State the preparation type.
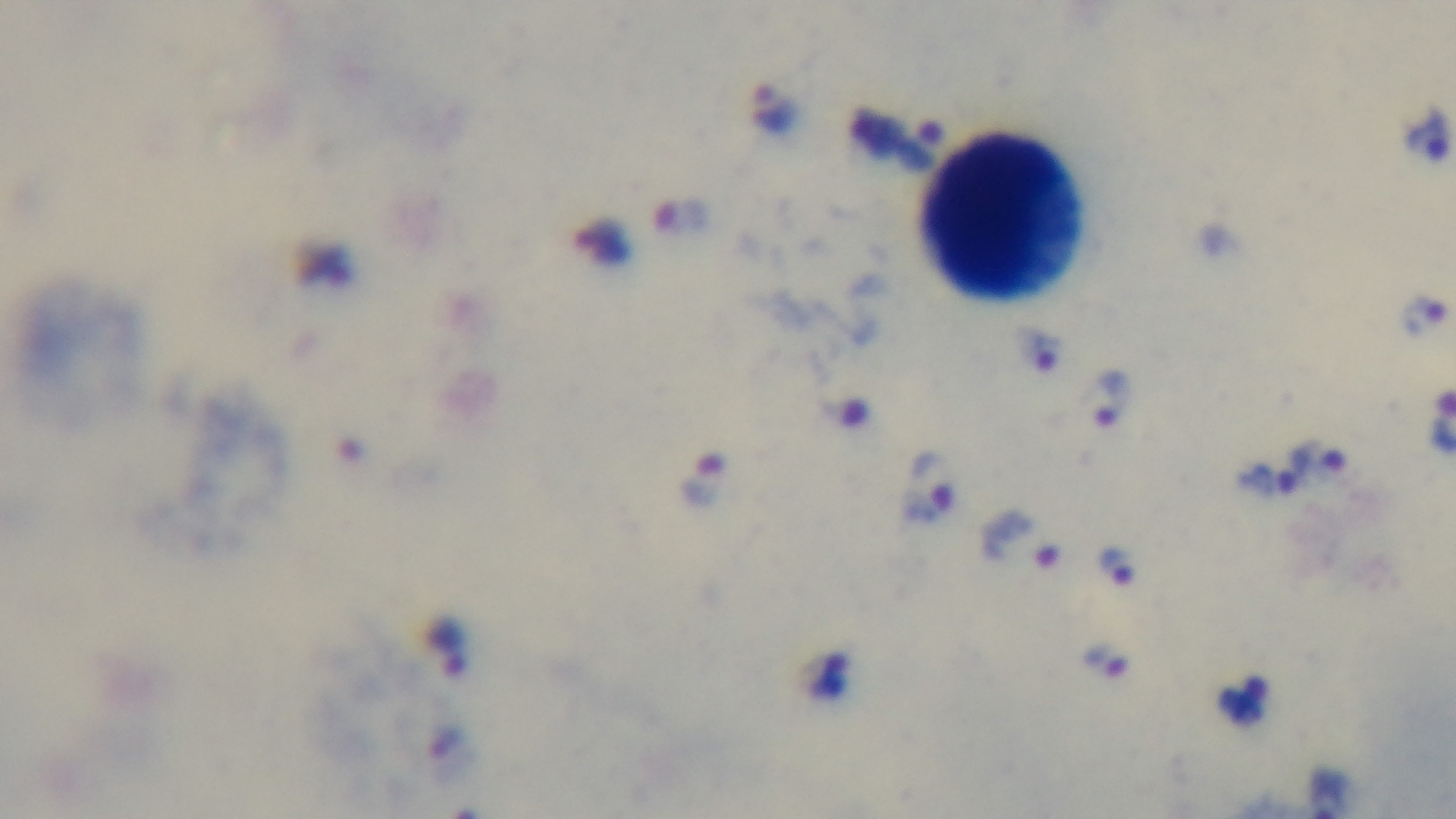

Thick.

Summary:
  - Capture: mounted 4K digital camera
  - Objective: 100x oil immersion
  - Field of view: one from the slide
  - Stain: Giemsa
  - Modality: light microscopy
  - Malaria status: infected